State which parasite is depicted.
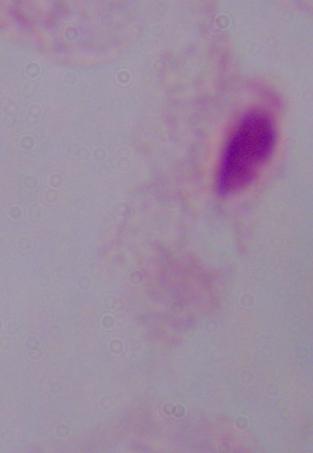

A trichomonad.

Captured at 1000x magnification. Micrograph.